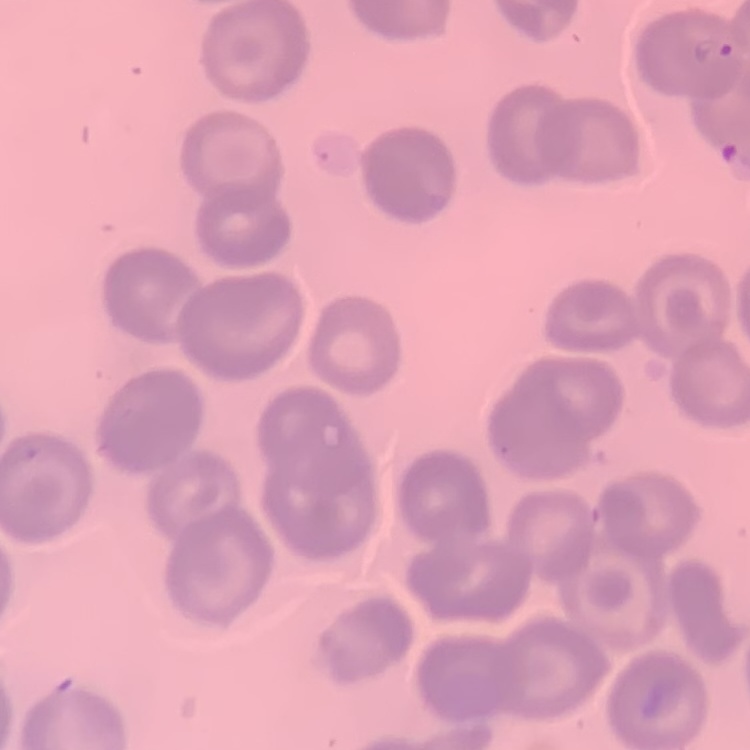
Summary:
  - Erythrocyte morphology: no rouleaux formation
  - Preparation: thin blood film
  - Stain: Field's or Giemsa
  - Image type: one tile cut from a larger photomicrograph